Name the cell type shown.
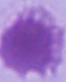

An erythrocyte.

1000x magnification. Photomicrograph.